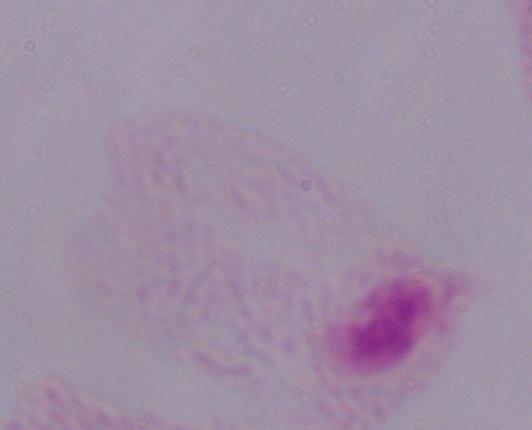

1000x magnification. A trichomonad is seen. Photomicrograph.